Locate every Plasmodium parasite and identify its life-cycle stage.
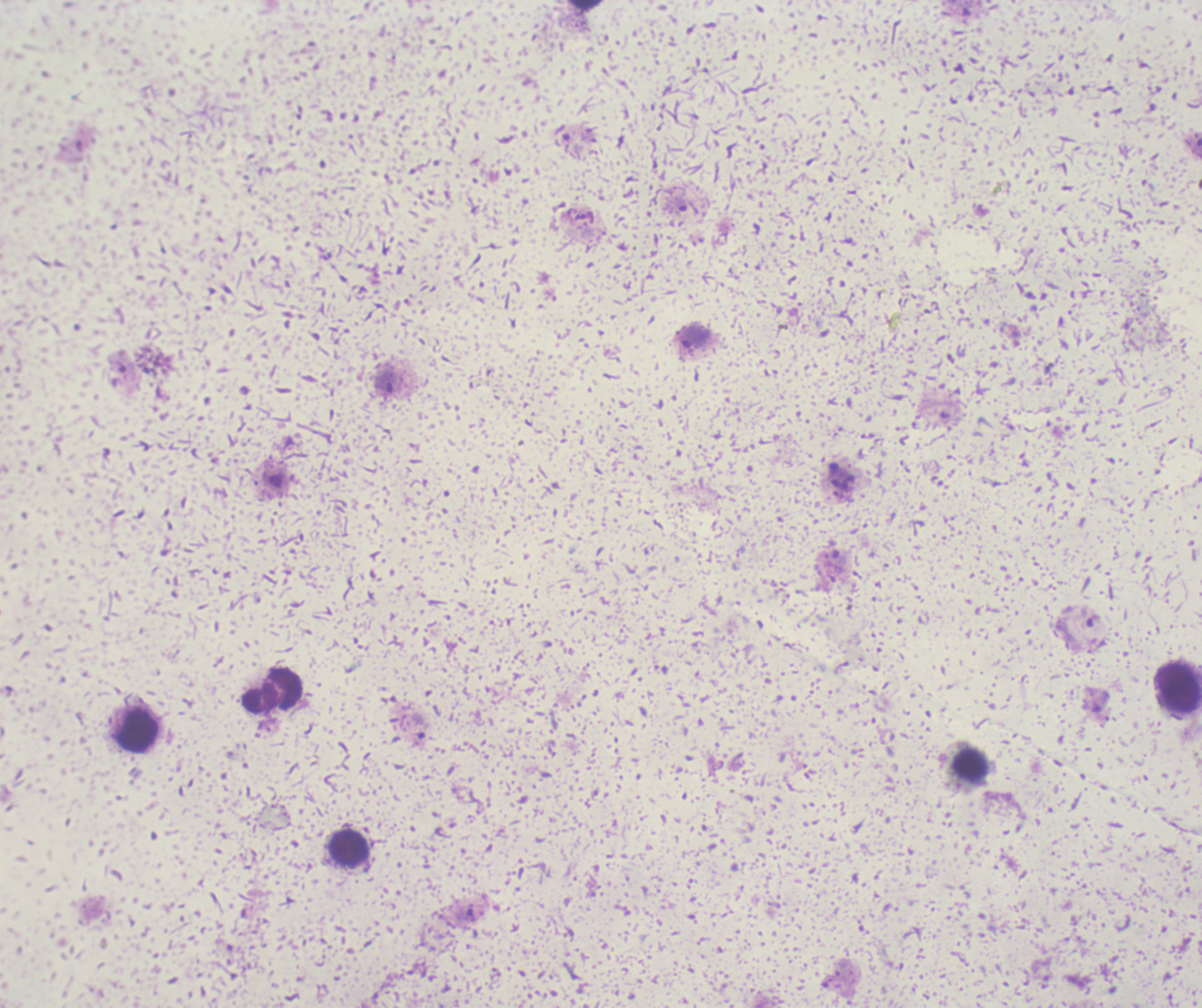
Approximate object centers, in pixels from the top-left corner.
Trophozoites: (x=679, y=203), (x=694, y=338), (x=384, y=382), (x=1077, y=630), (x=419, y=726).
No schizont or gametocyte forms observed.

Approximate object centers, in pixels from the top-left corner.
Summary:
  - Leukocyte locations: (x=585, y=6), (x=1177, y=690), (x=274, y=691), (x=137, y=732), (x=349, y=849)
  - Context: previously used in a real diagnosis
  - Magnification: 100x
  - Field of view: one from this slide
  - Image size: 1202×1008 pixels
  - Preparation: thick blood smear
  - Stain: Romanowsky
  - Background quality: unsatisfactory